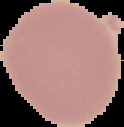 Image is 124×127 pixels. Result: no malaria parasites seen. The area outside the segmented cell region is set to black. From a thin blood smear.